Give the extent of all Plasmodium falciparum-infected red blood cells.
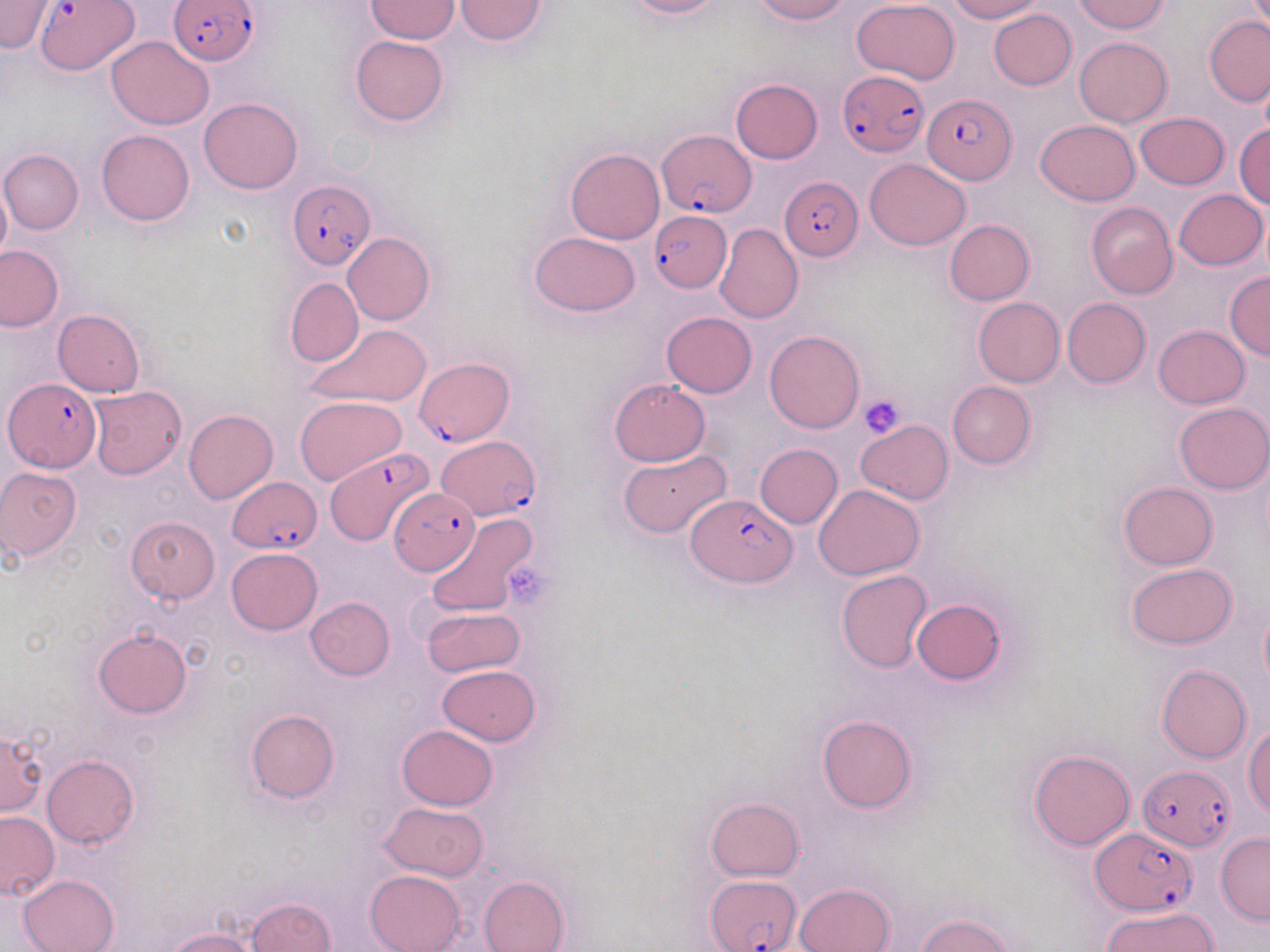

Approximate bounding boxes as named x1/y1/x2/y2 corners in pixels.
Plasmodium falciparum-infected red blood cells: (x1=169, y1=1, x2=262, y2=67), (x1=36, y1=2, x2=139, y2=77), (x1=839, y1=71, x2=925, y2=155), (x1=924, y1=95, x2=1013, y2=185), (x1=656, y1=129, x2=756, y2=217), (x1=782, y1=177, x2=863, y2=260), (x1=288, y1=179, x2=375, y2=270), (x1=649, y1=212, x2=729, y2=290), (x1=415, y1=357, x2=514, y2=448), (x1=3, y1=378, x2=99, y2=473), (x1=438, y1=436, x2=539, y2=519), (x1=326, y1=448, x2=438, y2=548), (x1=227, y1=476, x2=322, y2=553), (x1=390, y1=487, x2=481, y2=575), (x1=686, y1=492, x2=793, y2=588), (x1=1137, y1=764, x2=1234, y2=852), (x1=1090, y1=828, x2=1196, y2=915), (x1=709, y1=874, x2=802, y2=951).

Summary:
  - Platelet locations: (x1=860, y1=393, x2=907, y2=441), (x1=505, y1=557, x2=556, y2=606)
  - Uninfected red blood cell locations: (x1=454, y1=0, x2=549, y2=44), (x1=623, y1=0, x2=723, y2=19), (x1=750, y1=0, x2=852, y2=24), (x1=852, y1=0, x2=960, y2=85), (x1=946, y1=0, x2=1045, y2=23), (x1=1073, y1=0, x2=1170, y2=34), (x1=0, y1=1, x2=54, y2=52), (x1=366, y1=1, x2=459, y2=43), (x1=988, y1=8, x2=1076, y2=89), (x1=1204, y1=15, x2=1270, y2=106), (x1=106, y1=36, x2=215, y2=130), (x1=350, y1=36, x2=447, y2=126), (x1=1074, y1=37, x2=1172, y2=128), (x1=1257, y1=74, x2=1270, y2=148), (x1=730, y1=79, x2=823, y2=164), (x1=199, y1=98, x2=303, y2=194), (x1=1135, y1=112, x2=1230, y2=190), (x1=1037, y1=119, x2=1140, y2=205), (x1=1233, y1=124, x2=1270, y2=207), (x1=328, y1=128, x2=375, y2=178), (x1=96, y1=129, x2=194, y2=226), (x1=565, y1=147, x2=664, y2=244), (x1=0, y1=148, x2=85, y2=234), (x1=864, y1=158, x2=971, y2=249), (x1=0, y1=179, x2=11, y2=264), (x1=1173, y1=189, x2=1267, y2=270), (x1=1084, y1=202, x2=1178, y2=299), (x1=944, y1=219, x2=1034, y2=305), (x1=716, y1=223, x2=803, y2=323), (x1=530, y1=232, x2=641, y2=316), (x1=343, y1=233, x2=435, y2=325), (x1=0, y1=245, x2=65, y2=332), (x1=1224, y1=272, x2=1269, y2=360), (x1=285, y1=277, x2=364, y2=368), (x1=1062, y1=297, x2=1151, y2=388), (x1=972, y1=298, x2=1064, y2=387), (x1=53, y1=309, x2=145, y2=397), (x1=660, y1=311, x2=757, y2=398), (x1=304, y1=323, x2=432, y2=408), (x1=1154, y1=325, x2=1250, y2=408), (x1=765, y1=330, x2=864, y2=434), (x1=609, y1=378, x2=711, y2=467), (x1=946, y1=381, x2=1036, y2=469), (x1=86, y1=386, x2=187, y2=479), (x1=295, y1=396, x2=406, y2=486), (x1=1174, y1=402, x2=1270, y2=494), (x1=183, y1=409, x2=278, y2=504), (x1=856, y1=421, x2=953, y2=503), (x1=755, y1=443, x2=842, y2=529), (x1=618, y1=450, x2=732, y2=540), (x1=0, y1=467, x2=83, y2=561), (x1=1119, y1=481, x2=1218, y2=569), (x1=814, y1=484, x2=923, y2=579), (x1=425, y1=513, x2=537, y2=619), (x1=126, y1=517, x2=220, y2=604), (x1=226, y1=548, x2=323, y2=635), (x1=1127, y1=563, x2=1238, y2=648), (x1=836, y1=571, x2=933, y2=673), (x1=305, y1=597, x2=394, y2=681), (x1=911, y1=597, x2=1006, y2=686), (x1=421, y1=608, x2=525, y2=678), (x1=1260, y1=608, x2=1270, y2=687), (x1=93, y1=628, x2=193, y2=718), (x1=1156, y1=663, x2=1251, y2=762), (x1=436, y1=664, x2=540, y2=746), (x1=245, y1=709, x2=339, y2=803), (x1=817, y1=714, x2=918, y2=813), (x1=397, y1=724, x2=498, y2=810), (x1=1246, y1=724, x2=1270, y2=820), (x1=0, y1=731, x2=47, y2=816), (x1=1028, y1=748, x2=1136, y2=851), (x1=42, y1=754, x2=139, y2=849), (x1=706, y1=796, x2=805, y2=880), (x1=379, y1=801, x2=488, y2=881), (x1=0, y1=811, x2=58, y2=899), (x1=1216, y1=833, x2=1269, y2=925), (x1=365, y1=870, x2=465, y2=952), (x1=19, y1=874, x2=119, y2=952), (x1=479, y1=876, x2=569, y2=952), (x1=795, y1=882, x2=895, y2=952), (x1=245, y1=897, x2=336, y2=951), (x1=1102, y1=906, x2=1220, y2=952), (x1=914, y1=913, x2=1017, y2=952), (x1=166, y1=928, x2=260, y2=952)
  - Slide-level diagnosis: Plasmodium falciparum
  - Magnification: 1000x
  - Stain: May-Grünwald-Giemsa
  - Image size: 1270×952 pixels
  - Field of view: single
  - Preparation: thin blood film
  - Modality: optical microscopy